Give the extent of all uninfected red blood cells.
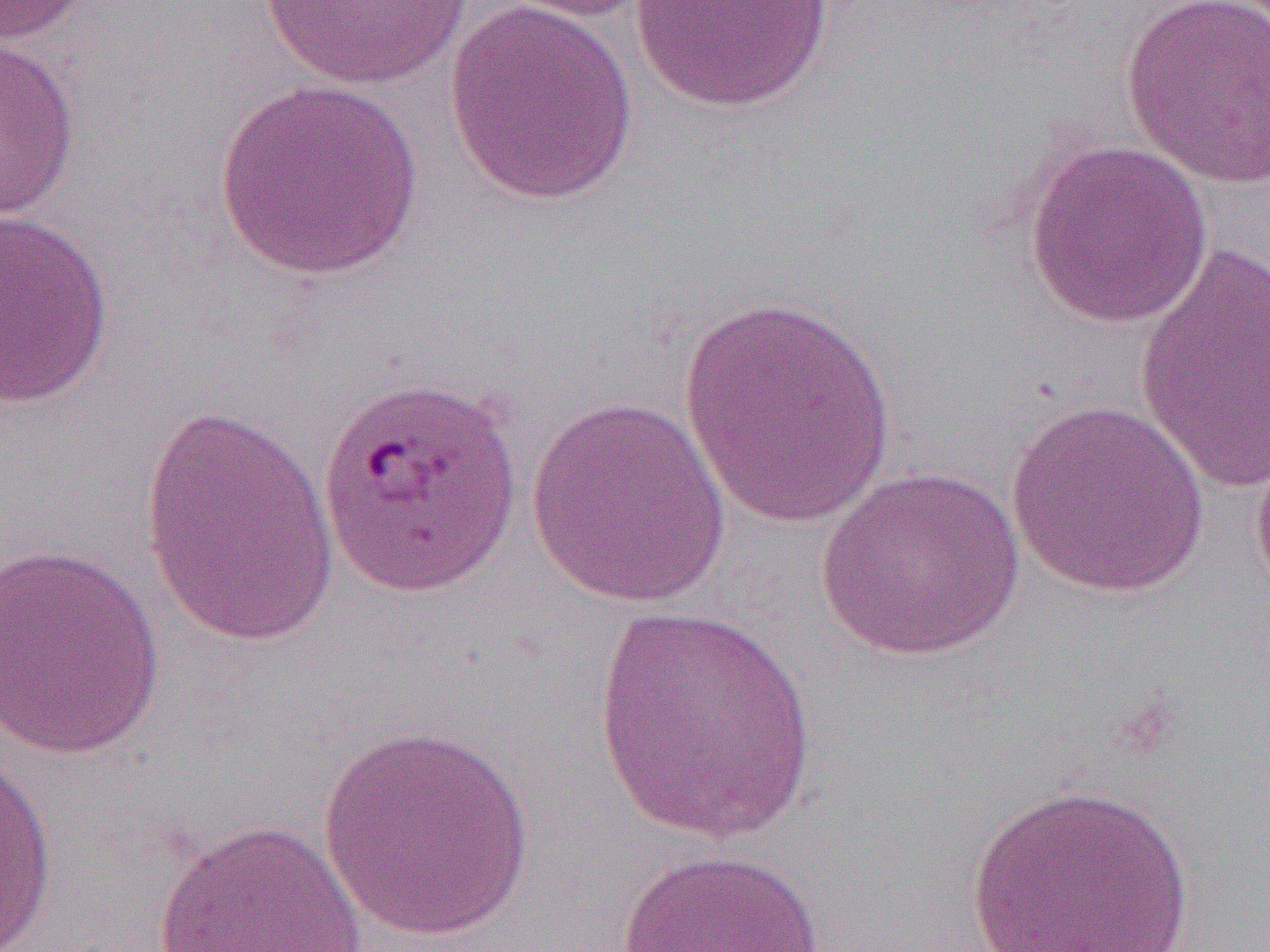
Approximate bounding boxes as named x1/y1/x2/y2 corners in pixels.
Uninfected red blood cells: (x1=0, y1=0, x2=94, y2=45), (x1=259, y1=0, x2=473, y2=90), (x1=486, y1=0, x2=658, y2=24), (x1=629, y1=0, x2=837, y2=113), (x1=1120, y1=0, x2=1270, y2=190), (x1=443, y1=1, x2=642, y2=206), (x1=0, y1=36, x2=82, y2=224), (x1=212, y1=79, x2=428, y2=283), (x1=1021, y1=139, x2=1213, y2=329), (x1=0, y1=209, x2=115, y2=409), (x1=1133, y1=240, x2=1269, y2=497), (x1=677, y1=291, x2=900, y2=533), (x1=525, y1=397, x2=733, y2=609), (x1=137, y1=399, x2=338, y2=648), (x1=1004, y1=399, x2=1211, y2=598), (x1=1250, y1=429, x2=1270, y2=608), (x1=815, y1=467, x2=1025, y2=662), (x1=0, y1=543, x2=166, y2=761), (x1=589, y1=605, x2=821, y2=845), (x1=315, y1=724, x2=537, y2=942), (x1=0, y1=749, x2=59, y2=952), (x1=967, y1=783, x2=1195, y2=952), (x1=151, y1=818, x2=369, y2=952), (x1=611, y1=848, x2=836, y2=952).

Summary:
  - Slide-level diagnosis: Plasmodium falciparum
  - Modality: optical microscopy
  - Image size: 1270×952 pixels
  - Preparation: thin blood film
  - Magnification: 1000x
  - Field of view: one of a larger specimen